Locate every blood parasite and identify its species.
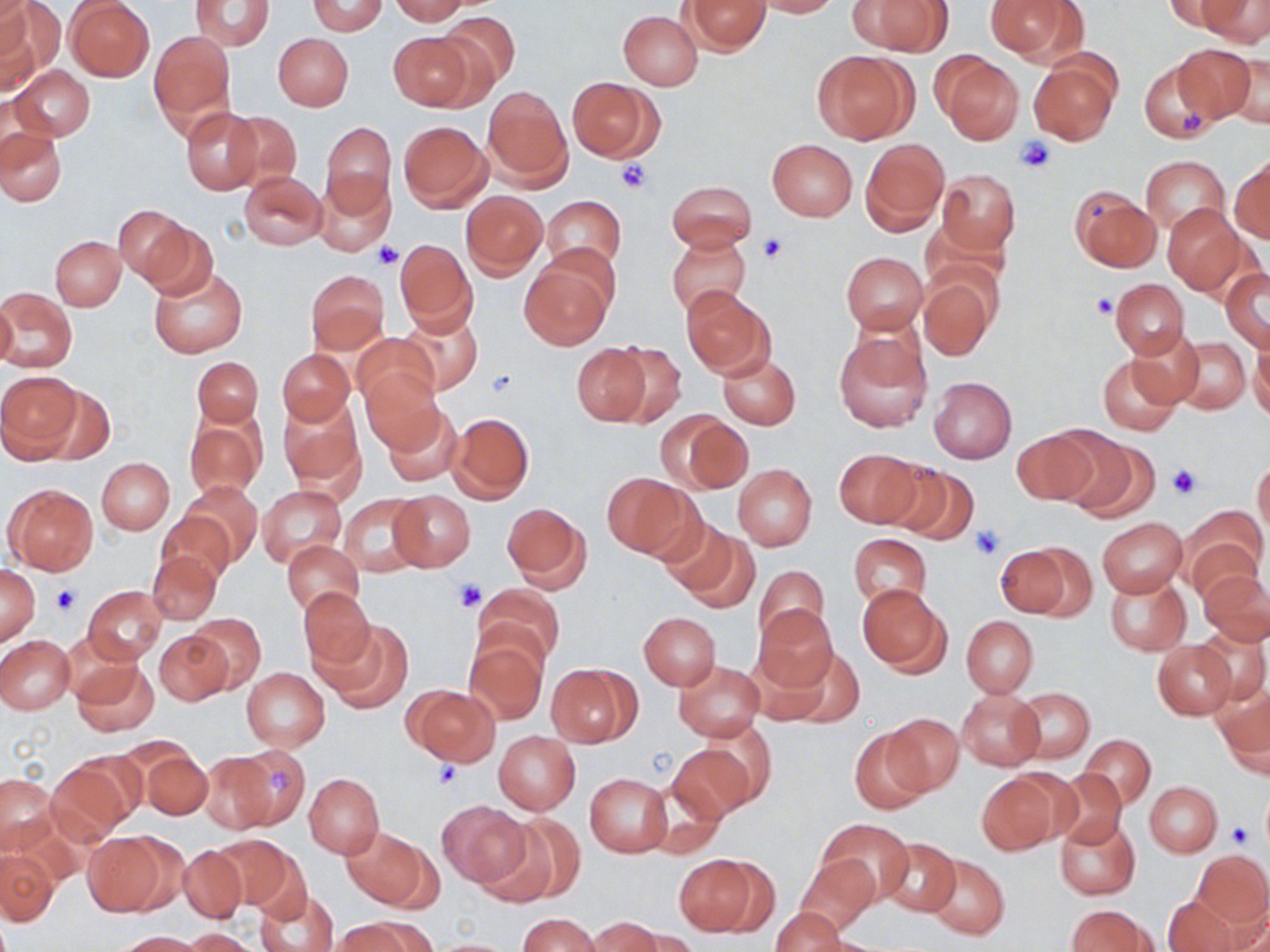

No blood parasites observed.

slide-level diagnosis = no evidence of blood parasites
platelet locations = approximate bounding boxes as [x1, y1, x2, y2] in pixels: [1180, 108, 1205, 137], [1016, 136, 1057, 173], [616, 159, 651, 194], [758, 235, 788, 263], [374, 240, 402, 269], [1090, 293, 1117, 318], [488, 369, 518, 399], [1168, 463, 1203, 500], [970, 523, 1005, 559], [455, 579, 487, 612], [52, 584, 80, 615], [431, 760, 462, 791], [1226, 823, 1251, 847]
stain = May-Grünwald-Giemsa
uninfected red blood cell locations = approximate bounding boxes as [x1, y1, x2, y2] in pixels: [1, 0, 30, 55], [308, 0, 386, 35], [388, 0, 473, 24], [754, 0, 840, 17], [852, 0, 953, 56], [984, 0, 1086, 65], [1163, 0, 1242, 31], [1194, 0, 1270, 43], [65, 1, 155, 82], [190, 1, 273, 51], [682, 1, 769, 53], [0, 2, 60, 88], [437, 10, 519, 93], [619, 11, 703, 90], [387, 30, 476, 110], [149, 31, 234, 132], [274, 33, 353, 110], [1171, 43, 1258, 126], [812, 49, 916, 144], [1217, 50, 1270, 130], [937, 53, 1023, 144], [1028, 56, 1120, 145], [1137, 56, 1223, 143], [10, 65, 95, 141], [567, 76, 659, 160], [482, 86, 571, 187], [0, 93, 56, 168], [181, 107, 263, 194], [224, 109, 302, 191], [399, 120, 492, 212], [320, 121, 395, 214], [0, 127, 66, 206], [860, 138, 948, 234], [767, 139, 857, 221], [1141, 155, 1229, 237], [1230, 158, 1270, 243], [240, 170, 328, 250], [937, 170, 1019, 255], [315, 176, 394, 257], [666, 180, 756, 250], [1068, 187, 1160, 272], [461, 191, 547, 276], [541, 195, 627, 273], [1164, 204, 1245, 294], [113, 205, 191, 285], [137, 217, 218, 300], [666, 232, 751, 318], [51, 237, 125, 310], [394, 238, 477, 332], [547, 242, 623, 319], [841, 252, 928, 333], [518, 260, 613, 350], [147, 264, 248, 359], [1221, 267, 1270, 350], [306, 270, 390, 354], [918, 273, 996, 361], [1110, 278, 1189, 358], [0, 287, 77, 372], [682, 287, 774, 378], [1, 295, 18, 371], [399, 309, 483, 395], [833, 329, 931, 432], [1128, 330, 1202, 411], [351, 331, 439, 409], [1173, 338, 1250, 413], [607, 340, 687, 427], [572, 343, 649, 425], [1249, 343, 1270, 422], [277, 349, 355, 425], [717, 353, 800, 430], [1097, 355, 1182, 435], [192, 357, 264, 427], [360, 367, 444, 453], [0, 371, 80, 460], [928, 376, 1016, 463], [37, 383, 116, 465], [279, 397, 364, 491], [381, 402, 464, 487], [447, 412, 534, 502], [668, 413, 753, 493], [184, 414, 266, 501], [1047, 427, 1147, 517], [1011, 429, 1099, 507], [832, 448, 924, 527], [97, 457, 174, 534], [1253, 457, 1269, 539], [733, 464, 817, 550], [882, 464, 980, 547], [603, 472, 692, 559], [182, 480, 263, 564], [4, 481, 98, 575], [258, 485, 345, 565], [387, 490, 475, 571], [339, 493, 427, 577], [502, 501, 591, 591], [157, 510, 237, 586], [1184, 510, 1265, 598], [1098, 518, 1186, 596], [661, 521, 755, 608], [850, 534, 931, 611], [282, 540, 363, 615], [999, 543, 1092, 620], [147, 549, 221, 625], [753, 565, 831, 644], [0, 566, 40, 645], [1199, 569, 1270, 645], [1104, 572, 1190, 655], [858, 583, 950, 675], [475, 584, 560, 671], [84, 586, 166, 662], [297, 587, 377, 670], [754, 603, 839, 692], [188, 612, 265, 693], [639, 612, 720, 689], [961, 616, 1037, 696], [315, 619, 411, 712], [1197, 625, 1269, 706], [155, 630, 232, 705], [0, 635, 75, 714], [464, 638, 547, 724], [1153, 640, 1236, 719], [766, 644, 863, 724], [72, 658, 158, 736], [673, 661, 763, 741], [548, 663, 639, 748], [242, 667, 329, 749], [405, 685, 500, 766], [1215, 686, 1270, 775], [1011, 688, 1093, 765], [956, 689, 1045, 770], [884, 712, 965, 796], [700, 721, 778, 807], [848, 728, 931, 813], [494, 731, 580, 814], [1079, 734, 1155, 809], [225, 744, 311, 831], [667, 744, 756, 824], [141, 748, 213, 819], [198, 751, 276, 833], [45, 758, 136, 845], [1051, 769, 1126, 850], [304, 773, 384, 857], [585, 773, 671, 856], [1, 774, 59, 854], [976, 774, 1061, 854], [1145, 781, 1221, 856], [1260, 790, 1269, 853], [435, 800, 530, 889], [479, 812, 584, 907], [1055, 817, 1140, 899], [819, 820, 911, 899], [341, 828, 430, 909], [84, 834, 168, 914], [212, 835, 304, 913], [878, 837, 960, 916], [177, 844, 248, 923], [1192, 849, 1269, 928], [0, 850, 57, 927], [673, 853, 768, 935], [794, 854, 880, 935], [923, 854, 1009, 940], [256, 888, 339, 952], [1163, 894, 1241, 952], [1212, 898, 1270, 952], [1067, 905, 1151, 952], [770, 907, 847, 952], [519, 914, 599, 952], [335, 916, 434, 952], [585, 917, 663, 952], [181, 928, 262, 951], [621, 929, 700, 952], [117, 931, 207, 951], [421, 938, 524, 951]
field of view = single
image size = 1270×952 pixels
modality = light microscopy
preparation = thin blood film
magnification = 1000x